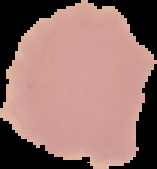

From a thin blood smear. Segmented cell region on a black background. Malaria status: uninfected. Image is 157×169 pixels.